Classify this cell by malaria status.
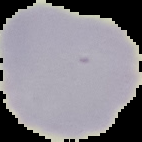

Uninfected.

Summary:
  - Image size: 142×142 pixels
  - Preparation: thin blood smear
  - Image type: segmented cell region with the area outside set to black